Look for Plasmodium parasites.
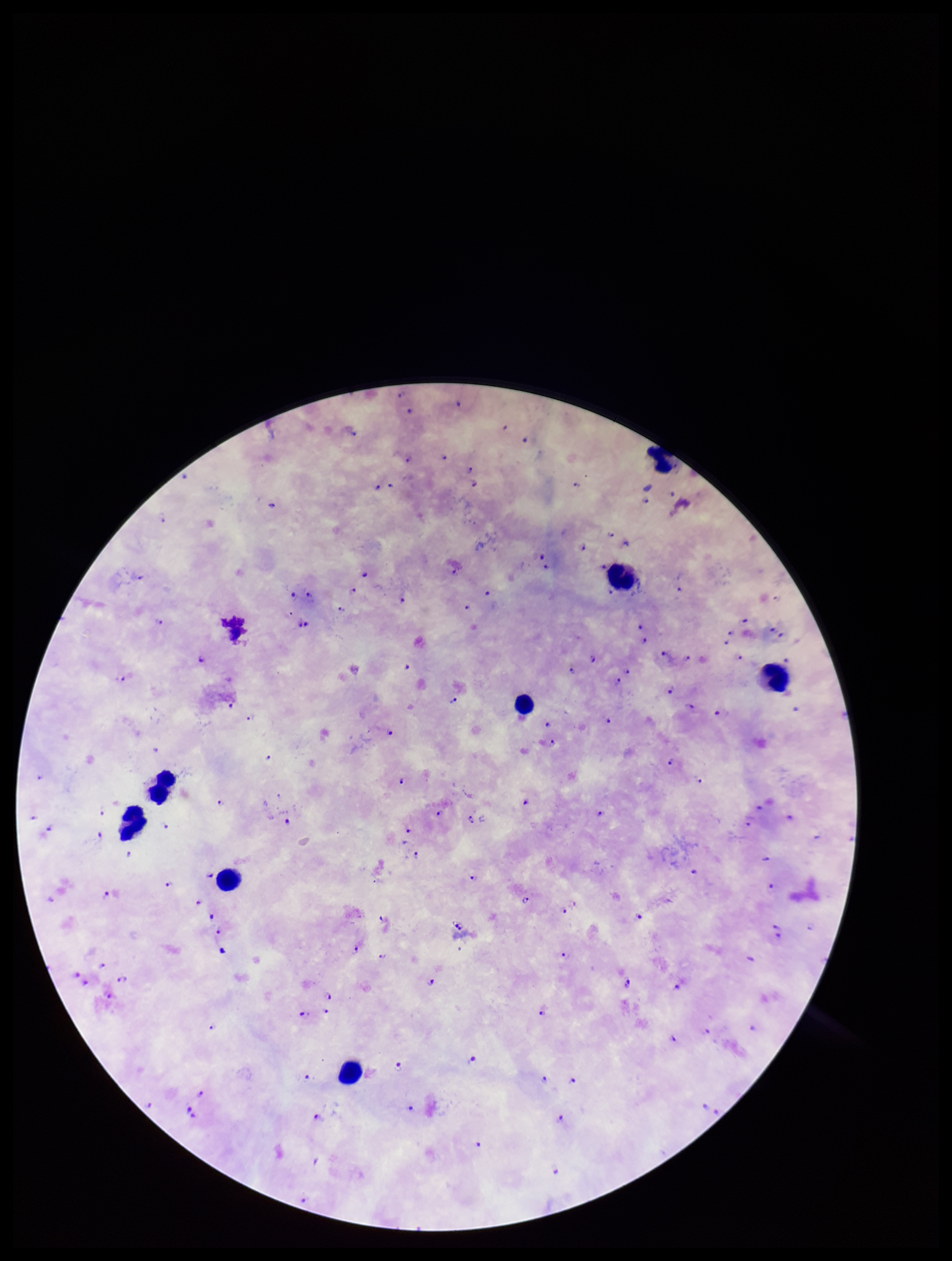

Identified.

Leukocyte count: 8. Image is 952×1261 pixels. Giemsa stain. Patient malaria status: positive. Preparation: thick blood smear. Single field of view. Smartphone photograph taken through the eyepiece of a microscope. Species reported for this patient: Plasmodium falciparum. Parasite count: 106.